Classify this cell by malaria status.
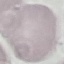

It is uninfected.

preparation = thin smear
image type = cell patch, automatically extracted from a larger field of view and resized to 64 × 64 pixels
stain = Giemsa
capture = smartphone through the microscope eyepiece